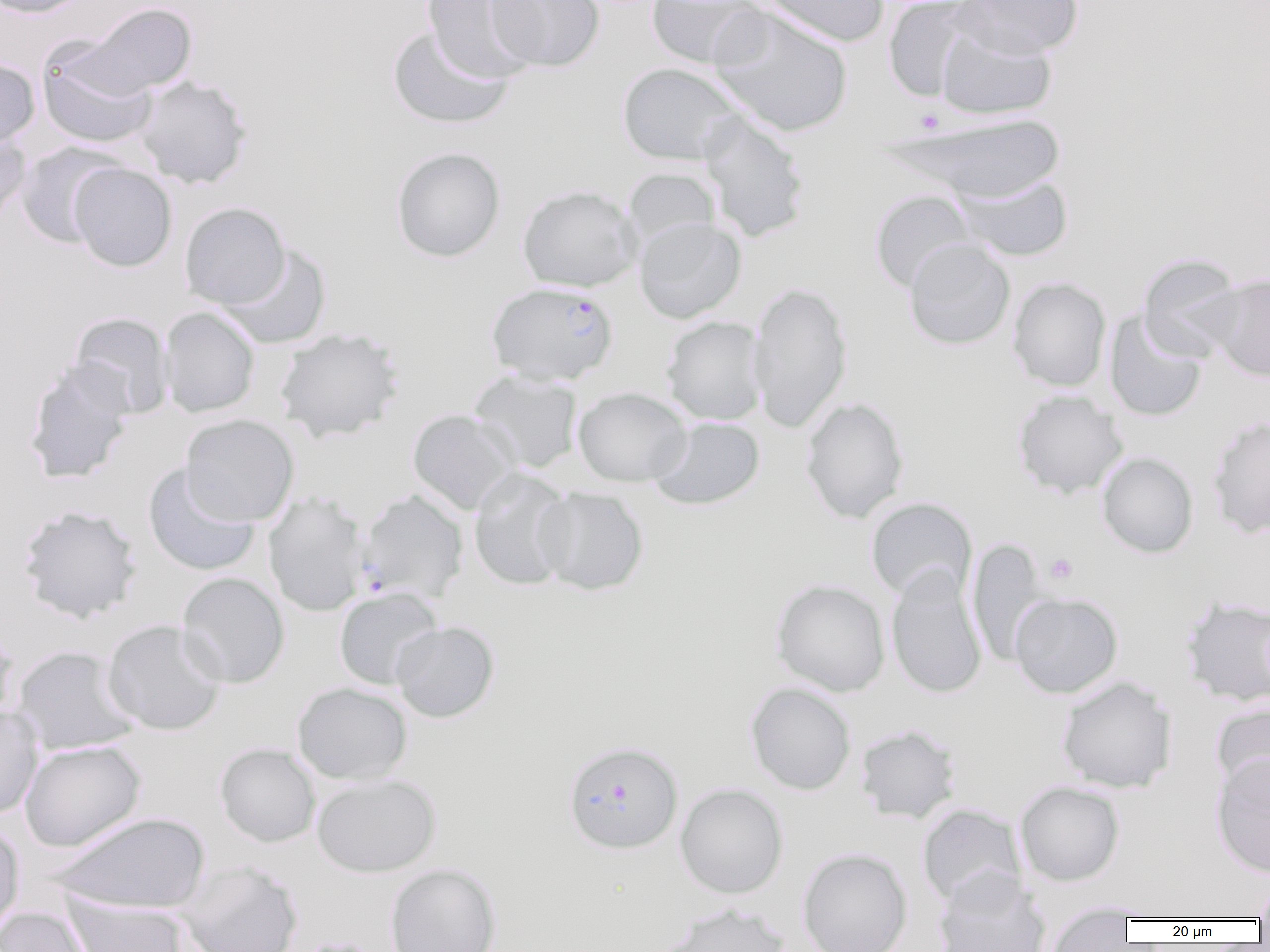
slide_level_diagnosis: Plasmodium falciparum
field_of_view: one of a larger specimen
image_size: 1270×952 pixels
preparation: thin blood smear
uninfected_red_blood_cell_locations_subset: 'approximate bounding boxes as named x1/y1/x2/y2 corners in pixels: (x1=0, y1=0, x2=95, y2=19), (x1=421, y1=0, x2=541, y2=83), (x1=486, y1=0, x2=605, y2=72), (x1=646, y1=0, x2=769, y2=70), (x1=757, y1=0, x2=888, y2=47), (x1=883, y1=0, x2=980, y2=102), (x1=955, y1=0, x2=1083, y2=58), (x1=76, y1=2, x2=197, y2=97), (x1=708, y1=7, x2=853, y2=138), (x1=935, y1=22, x2=1057, y2=120), (x1=387, y1=26, x2=514, y2=129), (x1=37, y1=44, x2=158, y2=149), (x1=0, y1=57, x2=40, y2=150), (x1=617, y1=63, x2=745, y2=166), (x1=134, y1=75, x2=252, y2=189), (x1=698, y1=112, x2=810, y2=242), (x1=881, y1=113, x2=1067, y2=203), (x1=0, y1=127, x2=31, y2=228), (x1=15, y1=142, x2=125, y2=249), (x1=391, y1=146, x2=506, y2=263), (x1=69, y1=162, x2=177, y2=272), (x1=622, y1=167, x2=722, y2=254), (x1=954, y1=174, x2=1074, y2=262), (x1=517, y1=185, x2=641, y2=292), (x1=868, y1=190, x2=979, y2=293), (x1=179, y1=202, x2=291, y2=310), (x1=634, y1=216, x2=746, y2=324), (x1=903, y1=239, x2=1015, y2=350), (x1=218, y1=244, x2=332, y2=348), (x1=1138, y1=254, x2=1247, y2=362), (x1=1207, y1=273, x2=1270, y2=382), (x1=1007, y1=277, x2=1112, y2=392), (x1=747, y1=281, x2=853, y2=434), (x1=159, y1=307, x2=260, y2=418), (x1=1105, y1=311, x2=1207, y2=422), (x1=68, y1=312, x2=174, y2=418), (x1=662, y1=316, x2=768, y2=426), (x1=274, y1=327, x2=405, y2=442), (x1=23, y1=360, x2=135, y2=485), (x1=468, y1=370, x2=585, y2=474), (x1=573, y1=387, x2=692, y2=487), (x1=1012, y1=389, x2=1128, y2=498), (x1=800, y1=397, x2=909, y2=523), (x1=407, y1=409, x2=521, y2=516), (x1=180, y1=414, x2=299, y2=526), (x1=1206, y1=415, x2=1270, y2=539), (x1=649, y1=417, x2=765, y2=511), (x1=1097, y1=451, x2=1198, y2=558), (x1=143, y1=463, x2=261, y2=577), (x1=468, y1=468, x2=575, y2=591), (x1=534, y1=486, x2=649, y2=596), (x1=263, y1=492, x2=369, y2=617), (x1=865, y1=497, x2=977, y2=602), (x1=17, y1=504, x2=142, y2=623), (x1=967, y1=539, x2=1050, y2=666), (x1=886, y1=565, x2=988, y2=700), (x1=177, y1=572, x2=290, y2=688), (x1=771, y1=579, x2=891, y2=697), (x1=334, y1=587, x2=443, y2=690), (x1=1009, y1=591, x2=1123, y2=699), (x1=102, y1=619, x2=227, y2=736), (x1=390, y1=621, x2=499, y2=723), (x1=0, y1=622, x2=20, y2=730), (x1=12, y1=645, x2=140, y2=756), (x1=1056, y1=676, x2=1177, y2=794), (x1=292, y1=682, x2=412, y2=785), (x1=745, y1=683, x2=856, y2=795), (x1=1211, y1=702, x2=1270, y2=805), (x1=0, y1=704, x2=44, y2=818), (x1=854, y1=724, x2=962, y2=824), (x1=19, y1=740, x2=146, y2=852), (x1=215, y1=743, x2=320, y2=848), (x1=1211, y1=752, x2=1270, y2=878), (x1=311, y1=774, x2=441, y2=877), (x1=1015, y1=781, x2=1125, y2=886), (x1=675, y1=783, x2=788, y2=899), (x1=917, y1=803, x2=1027, y2=909), (x1=49, y1=811, x2=212, y2=914), (x1=0, y1=822, x2=25, y2=936), (x1=797, y1=848, x2=913, y2=952), (x1=176, y1=859, x2=303, y2=952), (x1=385, y1=862, x2=502, y2=952), (x1=932, y1=869, x2=1051, y2=952), (x1=1254, y1=874, x2=1270, y2=922), (x1=65, y1=895, x2=190, y2=952), (x1=658, y1=903, x2=792, y2=952), (x1=1044, y1=905, x2=1136, y2=951), (x1=1, y1=906, x2=94, y2=952)'
plasmodium_falciparum_infected_red_blood_cell_locations_subset: 'approximate bounding boxes as named x1/y1/x2/y2 corners in pixels: (x1=486, y1=282, x2=619, y2=386), (x1=354, y1=489, x2=465, y2=605), (x1=562, y1=741, x2=683, y2=854)'
platelet_locations: 'approximate bounding boxes as named x1/y1/x2/y2 corners in pixels: (x1=914, y1=109, x2=945, y2=134), (x1=1044, y1=552, x2=1079, y2=585), (x1=296, y1=935, x2=382, y2=952)'
modality: optical microscopy
magnification: 1000x